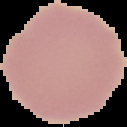
image type = cell region segmented out of the field of view; surrounding area masked to black
result = no malaria parasites detected
preparation = thin blood smear
image size = 127×127 pixels